Name the parasite shown.
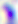

This is Toxoplasma gondii.

Photomicrograph. Captured at 400x magnification.